State which cell type is depicted.
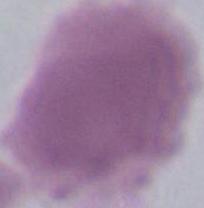

An erythrocyte.

1000x magnification. Photomicrograph.